Report the malaria status of this cell.
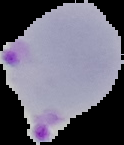
Parasitized.

The area outside the segmented cell region is set to black. From a thin blood smear. Image is 124×145 pixels.